Assess this cell for malaria.
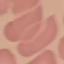
It is uninfected.

Giemsa-stained preparation. Acquired by smartphone through the microscope eyepiece. Automatically extracted cell patch, resized to 64 × 64 pixels. Thin blood smear.